Assess the morphology of the erythrocytes.
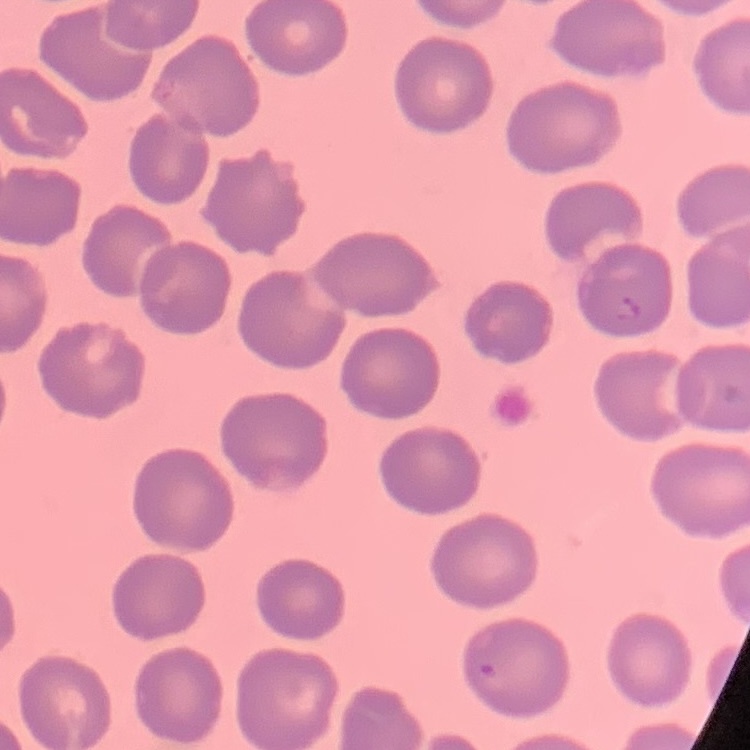

They show no rouleaux formation.

Square crop of a larger photomicrograph. Thin blood smear. Field's or Giemsa stain.